Report the malaria status of this cell.
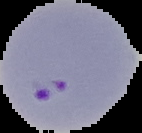
It is parasitized.

Segmented cell region on a black background. From a thin blood film. Image is 142×133 pixels.